Assess this cell for malaria.
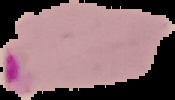
It is parasitized.

Summary:
  - Image size: 175×100 pixels
  - Image type: segmented cell region on a black background
  - Preparation: thin blood film